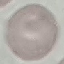
Summary:
  - Malaria status: uninfected
  - Capture: smartphone through the microscope eyepiece
  - Image type: cell patch, automatically extracted from a larger field of view and resized to 64 × 64 pixels
  - Stain: Giemsa
  - Preparation: thin smear